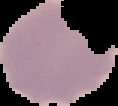
Malaria status: uninfected. Cell region segmented out of the field of view; the surrounding area is masked to black. From a thin blood film. Image is 118×106 pixels.